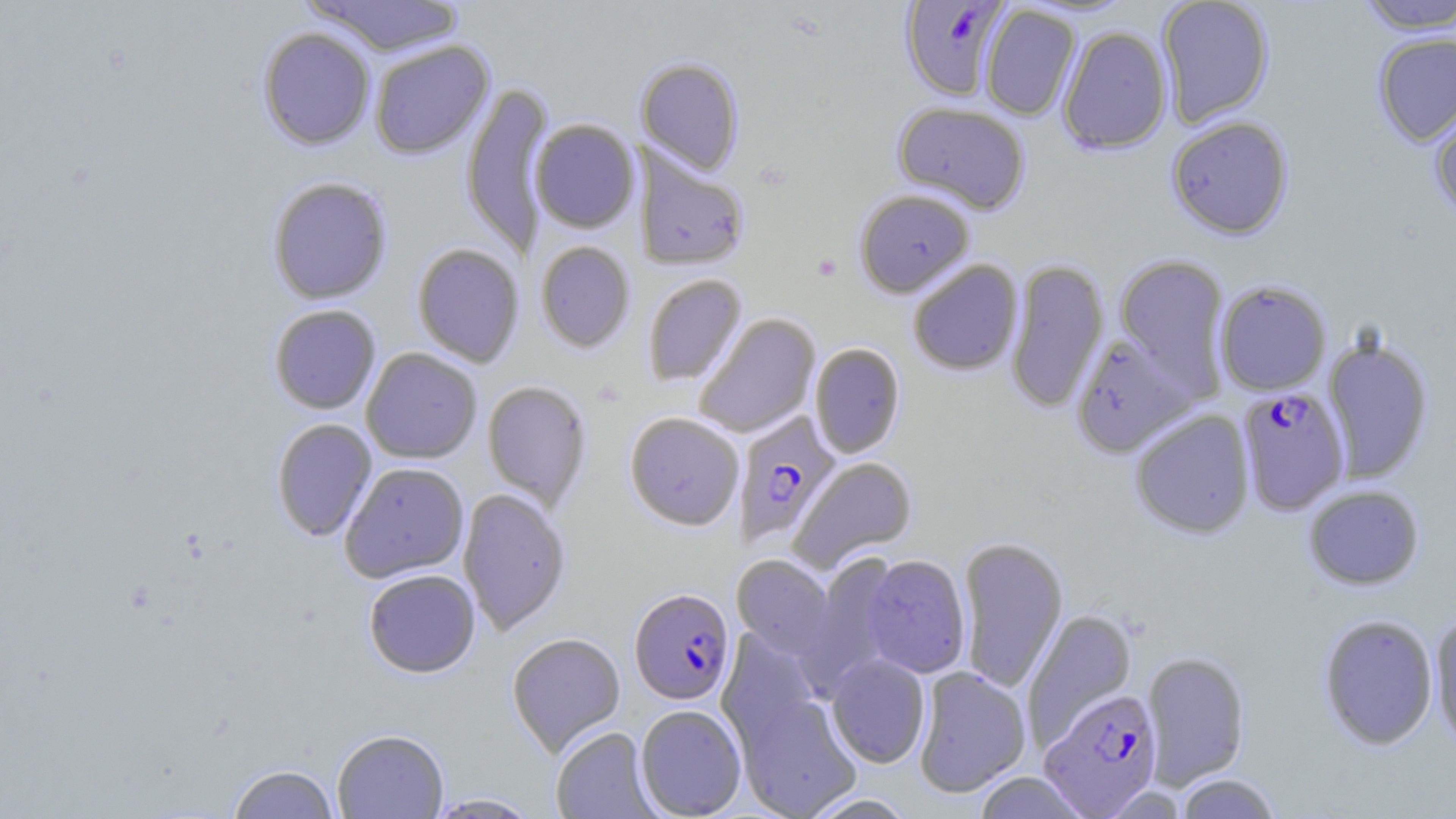
Approximate bounding boxes as (x1,y1)-(x2,y2) corner pairs in pixels. Plasmodium falciparum-infected red blood cell locations: (899,0)-(1011,101), (1236,386)-(1351,515), (733,411)-(841,547), (629,587)-(735,704), (1039,687)-(1163,817). Uninfected red blood cell locations: (303,0)-(466,56), (1156,0)-(1274,127), (1354,1)-(1456,33), (980,5)-(1081,121), (1057,25)-(1172,155), (257,26)-(376,151), (1372,32)-(1456,146), (368,39)-(494,159), (635,58)-(744,175), (460,81)-(554,258), (1428,99)-(1456,219), (892,102)-(1030,215), (1166,115)-(1293,239), (530,119)-(639,233), (634,146)-(749,272), (267,176)-(393,305), (854,189)-(975,297), (535,241)-(635,352), (411,243)-(525,368), (1114,253)-(1231,396), (908,259)-(1023,376), (1005,259)-(1110,414), (642,273)-(747,387), (1214,279)-(1331,396), (269,304)-(381,414), (694,313)-(820,438), (1069,333)-(1197,458), (1321,334)-(1434,483), (810,342)-(905,458), (360,347)-(482,464), (481,380)-(593,511), (1129,409)-(1255,539), (625,411)-(744,530), (270,418)-(378,541), (789,456)-(917,572), (339,462)-(469,583), (1303,485)-(1425,590), (458,487)-(571,636), (957,535)-(1068,693), (801,554)-(903,693), (861,554)-(971,678), (731,555)-(835,658), (363,568)-(480,678), (1022,609)-(1138,747), (1317,612)-(1439,751), (1429,612)-(1456,752), (717,629)-(825,750), (506,631)-(626,756), (1140,650)-(1251,788), (826,654)-(931,768), (913,667)-(1031,798), (732,689)-(863,819), (635,704)-(747,818), (550,726)-(659,818), (332,728)-(448,819), (227,764)-(340,818), (972,771)-(1090,818), (1174,774)-(1283,819), (425,793)-(541,818), (801,793)-(917,818). Platelet locations: (812,254)-(842,281). Slide-level diagnosis: Plasmodium falciparum. Optical microscopy. Single field of view. Image is 1456×819 pixels. Thin blood film. 1000x magnification. May-Grünwald-Giemsa stain.